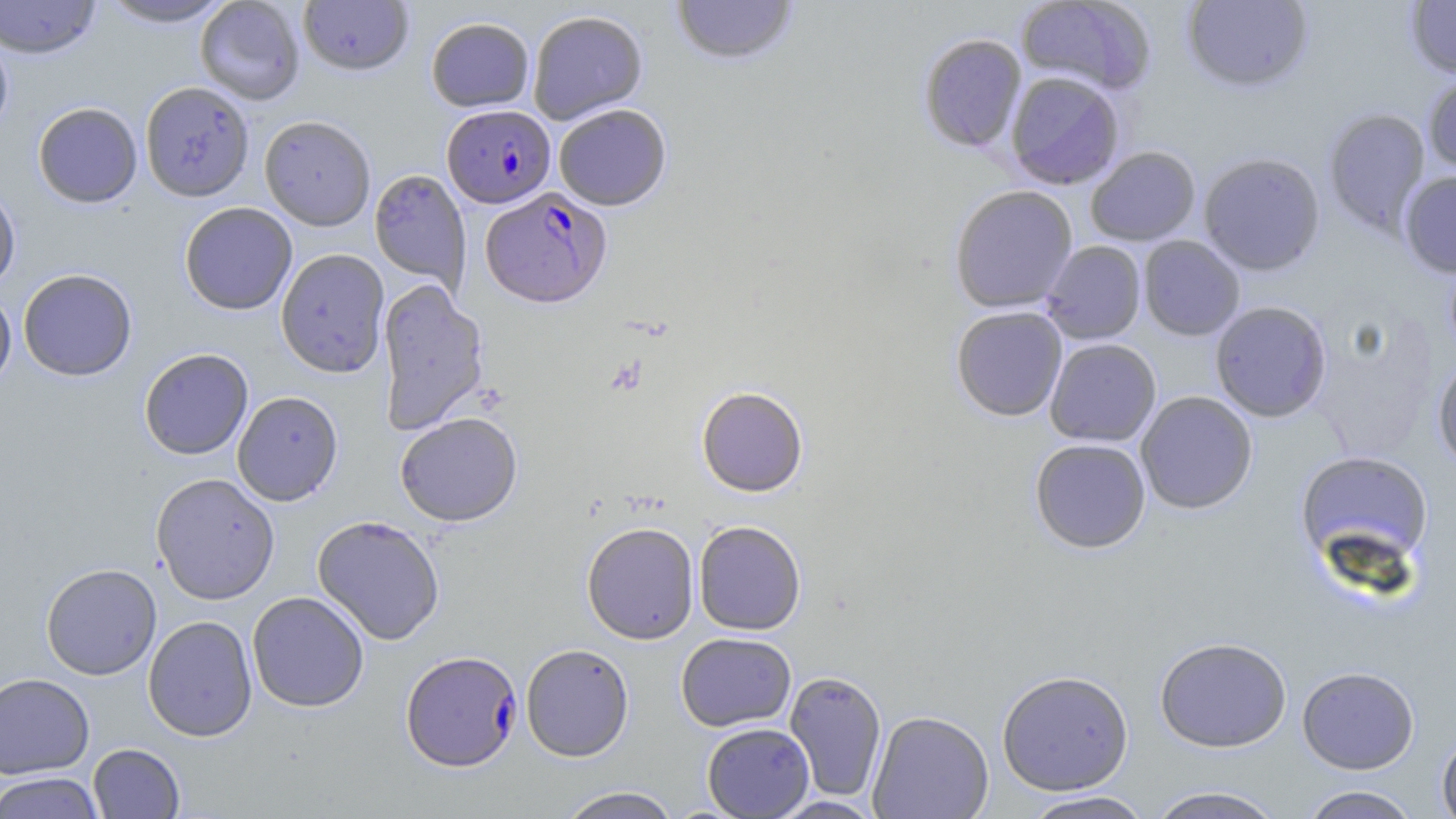

Summary:
  - Coordinate format: approximate bounding boxes as (x1, y1, x2, y2) in pixels
  - Plasmodium falciparum-infected red blood cell locations: (442, 104, 555, 208), (481, 187, 611, 309), (401, 650, 522, 772)
  - Uninfected red blood cell locations: (0, 0, 101, 59), (98, 0, 235, 28), (195, 0, 305, 105), (298, 0, 413, 76), (670, 0, 799, 67), (1016, 0, 1156, 94), (1181, 0, 1314, 93), (1404, 0, 1456, 79), (528, 11, 647, 124), (426, 16, 534, 112), (0, 30, 14, 140), (918, 33, 1027, 154), (1005, 71, 1125, 190), (1422, 71, 1456, 177), (139, 82, 254, 201), (33, 102, 142, 208), (553, 104, 672, 210), (1323, 108, 1431, 239), (259, 115, 376, 231), (1085, 146, 1200, 246), (1198, 152, 1326, 276), (369, 168, 470, 292), (1398, 170, 1456, 277), (0, 182, 20, 294), (949, 185, 1078, 313), (179, 202, 298, 315), (1138, 236, 1245, 340), (1041, 240, 1146, 344), (275, 248, 390, 377), (18, 269, 137, 381), (376, 279, 489, 436), (0, 289, 16, 395), (1210, 301, 1331, 422), (951, 306, 1068, 422), (1045, 338, 1161, 446), (139, 348, 253, 460), (1432, 356, 1456, 473), (696, 387, 808, 497), (1136, 390, 1257, 514), (232, 391, 343, 506), (394, 412, 523, 526), (1029, 438, 1151, 553), (1295, 451, 1434, 570), (150, 473, 280, 605), (312, 515, 446, 646), (693, 520, 806, 635), (581, 521, 699, 644), (41, 563, 162, 680), (247, 591, 369, 712), (143, 615, 258, 742), (676, 632, 797, 732), (1155, 637, 1292, 753), (520, 643, 634, 761), (1297, 666, 1419, 774), (784, 670, 887, 802), (996, 670, 1134, 796), (0, 672, 95, 779), (868, 710, 994, 819), (702, 723, 814, 819), (1436, 731, 1456, 819), (88, 743, 185, 818), (0, 772, 105, 819), (557, 786, 681, 818), (1145, 786, 1284, 819), (1298, 786, 1422, 819), (1020, 791, 1156, 818), (766, 795, 886, 818)
  - Slide-level diagnosis: Plasmodium falciparum
  - Preparation: thin blood film
  - Field of view: one of a larger specimen
  - Image size: 1456×819 pixels
  - Modality: optical microscopy
  - Magnification: 1000x
  - Stain: May-Grünwald-Giemsa